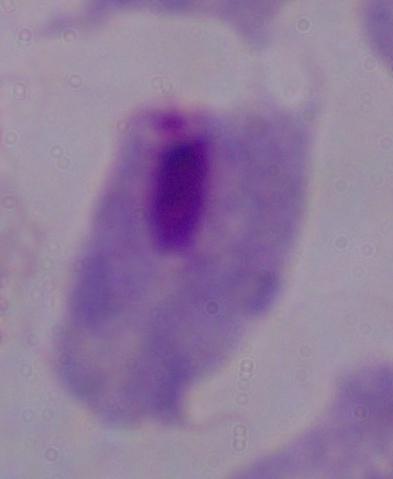
Summary:
  - Modality: photomicrograph
  - Identification: trichomonad
  - Magnification: 1000x